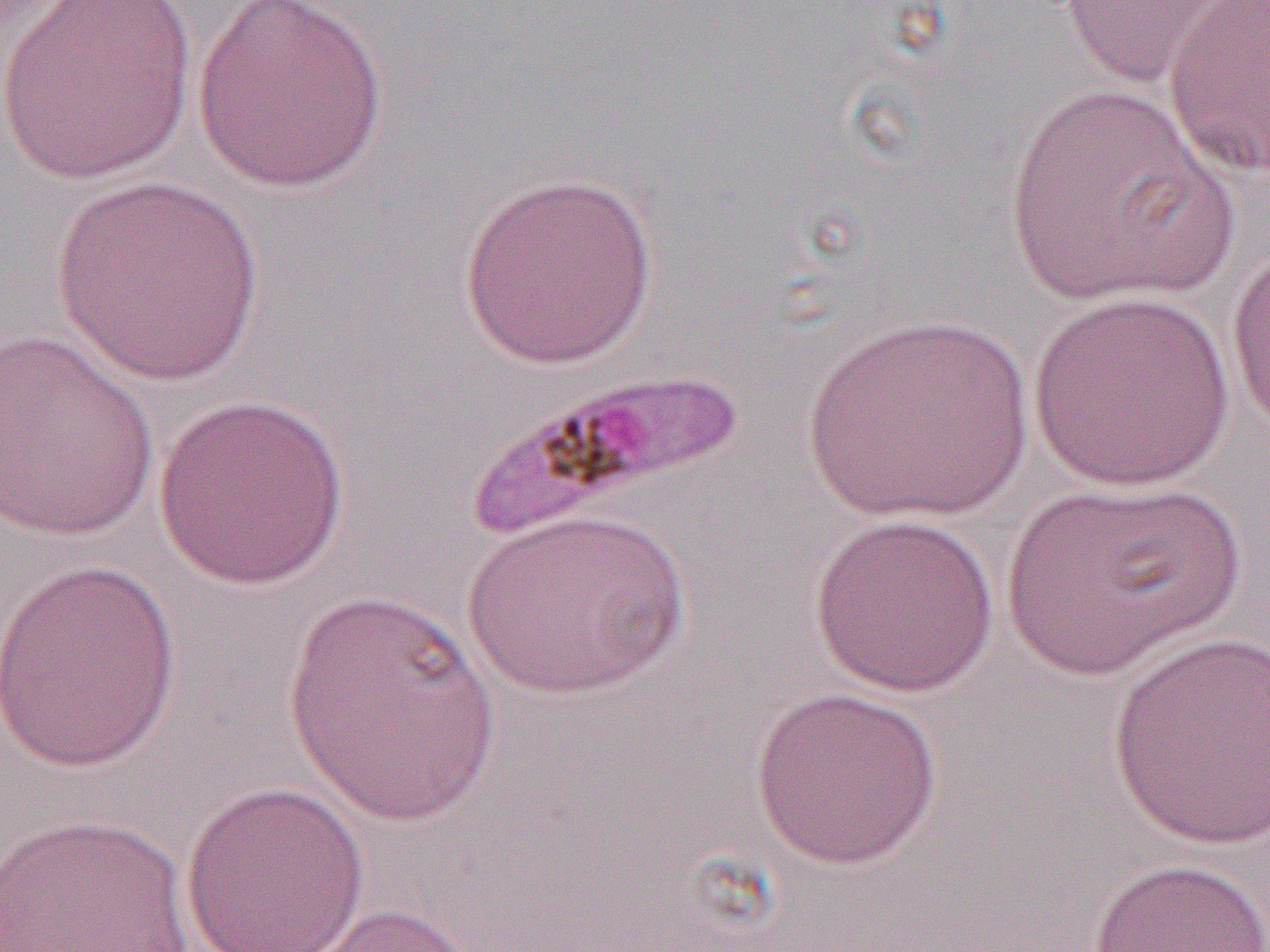

slide-level diagnosis = Plasmodium falciparum
field of view = one of a larger specimen
uninfected red blood cell locations = approximate bounding boxes as named x1/y1/x2/y2 corners in pixels: (x1=1, y1=0, x2=197, y2=186), (x1=192, y1=0, x2=389, y2=194), (x1=1055, y1=0, x2=1235, y2=89), (x1=1163, y1=1, x2=1270, y2=179), (x1=1004, y1=84, x2=1236, y2=309), (x1=459, y1=171, x2=657, y2=369), (x1=48, y1=175, x2=267, y2=386), (x1=1226, y1=242, x2=1270, y2=436), (x1=1026, y1=291, x2=1238, y2=492), (x1=800, y1=313, x2=1032, y2=523), (x1=0, y1=331, x2=160, y2=543), (x1=152, y1=392, x2=351, y2=590), (x1=1000, y1=478, x2=1247, y2=679), (x1=463, y1=509, x2=690, y2=699), (x1=808, y1=511, x2=1002, y2=699), (x1=0, y1=557, x2=183, y2=774), (x1=280, y1=585, x2=503, y2=830), (x1=1104, y1=633, x2=1270, y2=853), (x1=749, y1=684, x2=944, y2=871), (x1=180, y1=780, x2=371, y2=952), (x1=1, y1=812, x2=195, y2=951), (x1=1085, y1=856, x2=1270, y2=952), (x1=285, y1=900, x2=494, y2=952)
platelet locations = approximate bounding boxes as named x1/y1/x2/y2 corners in pixels: (x1=462, y1=366, x2=753, y2=539)
image size = 1270×952 pixels
magnification = 1000x
preparation = thin blood film
modality = optical microscopy